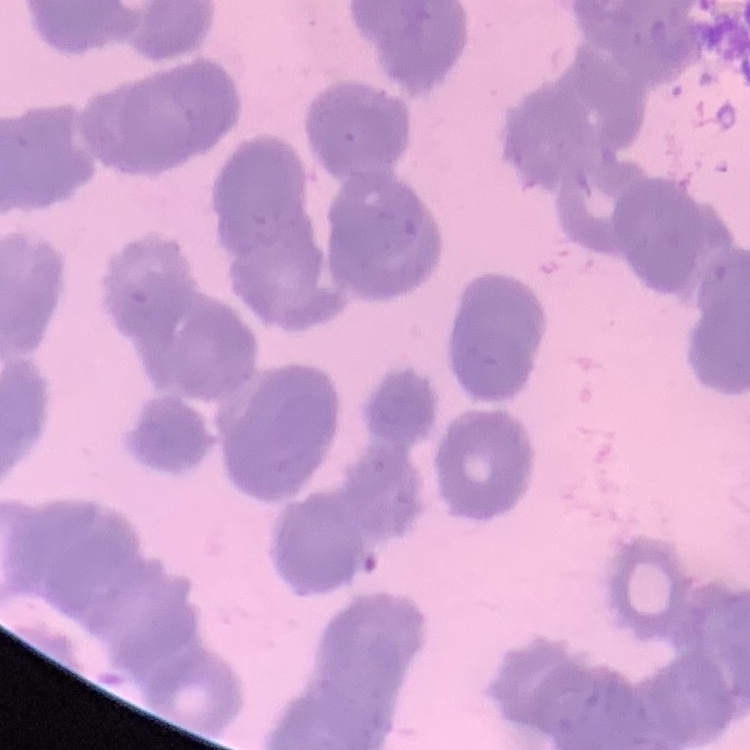
The erythrocytes exhibit rouleaux formation. Square crop of a larger photomicrograph. Stained with either Field's or Giemsa. Thin peripheral smear.